Identify the parasite.
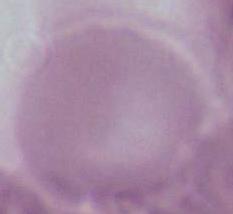

Plasmodium.

magnification: 400x or 1000x
modality: micrograph